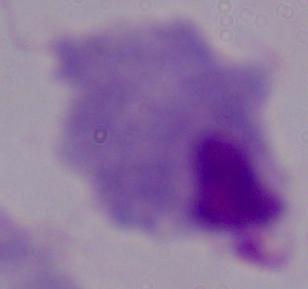
A trichomonad is shown. Photomicrograph. Captured at 1000x magnification.